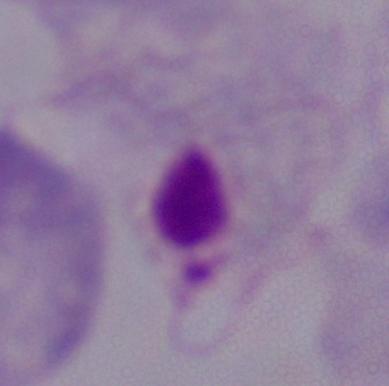

Summary:
  - Identification: trichomonad
  - Magnification: 1000x
  - Modality: micrograph